State which parasite is depicted.
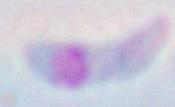

This is Toxoplasma gondii.

1000x magnification. Micrograph.